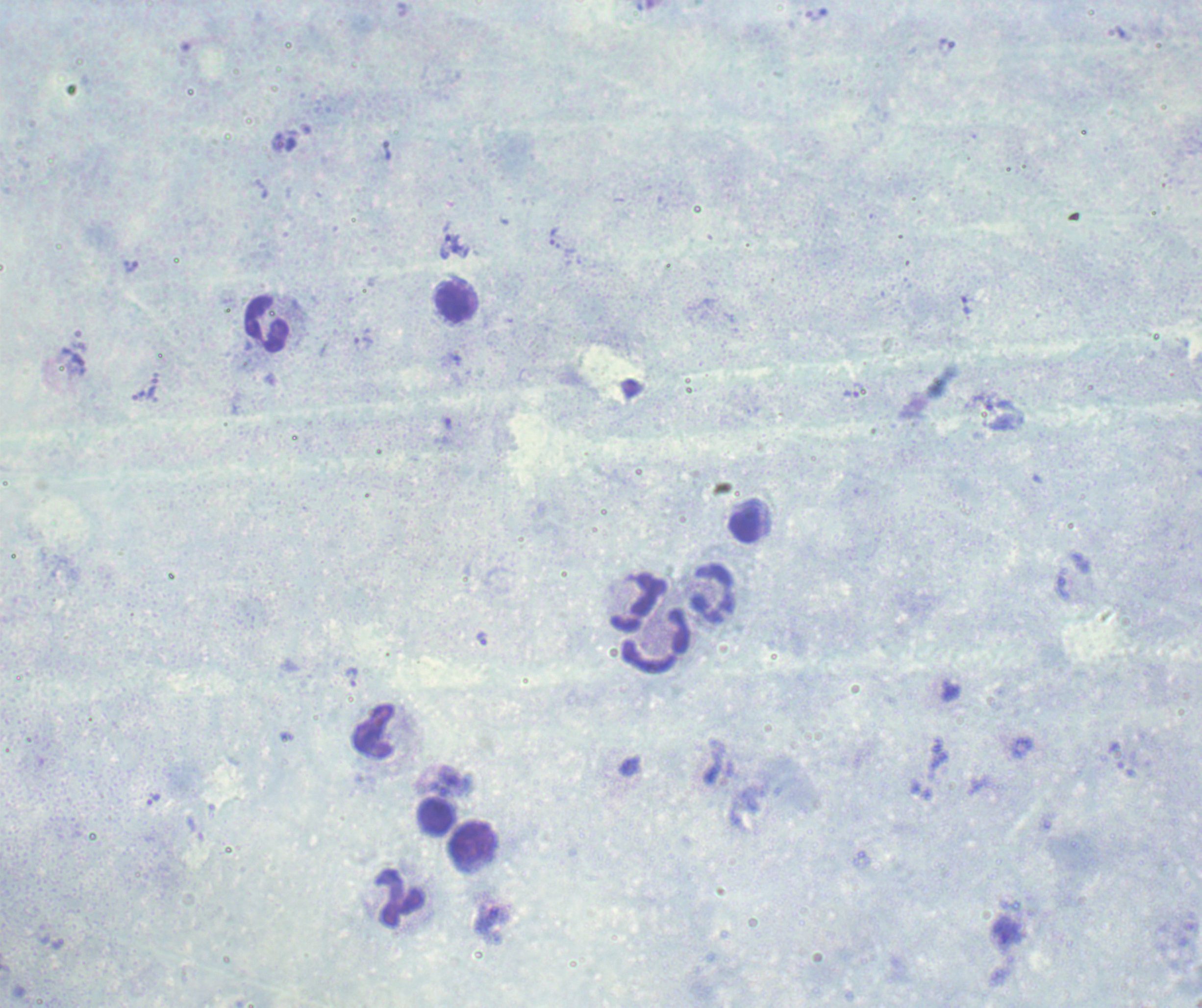 Thick blood smear. One field from this slide. Romanowsky stain. Image is 1202×1008 pixels.